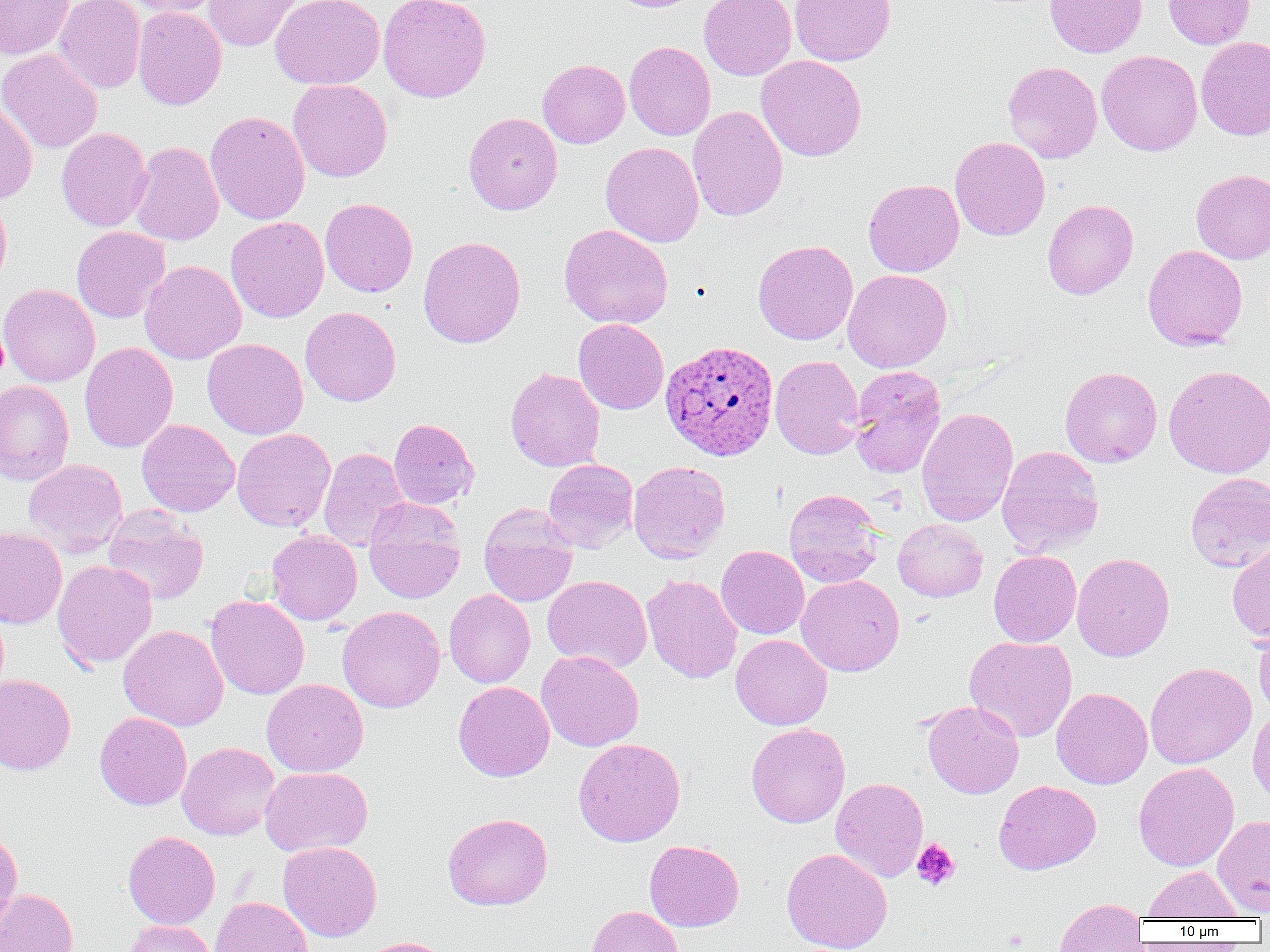
Approximate bounding boxes as (x1,y1)-(x2,y2) corner pairs in pixels. Plasmodium ovale-infected red blood cell locations: (660,339)-(779,461). Platelet locations: (911,838)-(960,890). Uninfected red blood cell locations: (0,0)-(74,60), (53,0)-(145,93), (119,0)-(222,17), (203,0)-(302,52), (270,0)-(385,90), (377,0)-(491,102), (605,0)-(702,12), (699,0)-(796,80), (790,0)-(896,66), (1044,0)-(1147,58), (1162,0)-(1255,49), (133,6)-(227,110), (1196,37)-(1270,140), (624,41)-(716,141), (0,48)-(103,153), (1097,50)-(1203,156), (756,55)-(867,162), (537,59)-(630,148), (1002,61)-(1103,163), (288,79)-(392,182), (0,97)-(37,205), (687,105)-(788,221), (205,111)-(310,225), (464,112)-(563,215), (56,127)-(152,231), (950,137)-(1050,241), (128,141)-(224,245), (600,142)-(704,247), (1191,169)-(1270,264), (863,179)-(964,276), (0,192)-(12,291), (320,198)-(418,297), (1042,199)-(1138,299), (226,217)-(328,323), (559,224)-(673,329), (71,226)-(170,323), (417,236)-(526,348), (753,240)-(858,345), (1143,244)-(1247,350), (139,259)-(247,365), (843,269)-(952,372), (0,284)-(100,387), (300,306)-(401,406), (573,319)-(669,414), (203,338)-(308,440), (79,342)-(178,453), (770,355)-(865,459), (1163,364)-(1270,478), (848,365)-(947,478), (1059,366)-(1162,468), (505,368)-(605,471), (0,380)-(74,486), (916,406)-(1018,527), (388,417)-(479,510), (137,419)-(240,517), (232,428)-(335,531), (996,445)-(1104,558), (318,447)-(409,552), (22,458)-(128,557), (543,459)-(638,552), (628,460)-(730,563), (1185,472)-(1270,573), (783,489)-(883,587), (363,497)-(465,604), (478,503)-(578,607), (102,507)-(209,605), (893,519)-(988,602), (0,526)-(67,629), (266,530)-(362,625), (1227,540)-(1270,644), (716,545)-(809,639), (989,550)-(1081,647), (1072,552)-(1175,662), (52,560)-(157,669), (642,574)-(742,683), (796,574)-(904,677), (542,575)-(653,672), (444,589)-(535,688), (206,595)-(309,700), (337,606)-(446,713), (1252,623)-(1270,720), (118,624)-(229,731), (731,634)-(832,730), (964,635)-(1077,742), (536,650)-(644,751), (1145,662)-(1256,769), (0,674)-(76,775), (262,679)-(368,777), (453,681)-(554,781), (1051,687)-(1153,789), (922,700)-(1024,799), (1248,709)-(1270,808), (94,712)-(192,810), (746,723)-(850,828), (573,738)-(686,847), (177,742)-(280,841), (1133,762)-(1239,872), (259,767)-(373,857), (830,777)-(929,882), (993,780)-(1101,875), (442,812)-(553,910), (1212,814)-(1270,916), (0,825)-(23,935), (122,831)-(220,929), (644,840)-(744,931), (278,841)-(382,942), (781,848)-(893,952), (1143,866)-(1244,920), (0,888)-(79,952), (210,896)-(313,952), (1053,897)-(1148,952), (586,905)-(684,952), (123,920)-(218,952), (354,936)-(455,952). Slide-level diagnosis: Plasmodium ovale. Single field of view. Image is 1270×952 pixels. Captured at 1000x magnification. Light microscopy. Thin blood film.